State the blood parasite species.
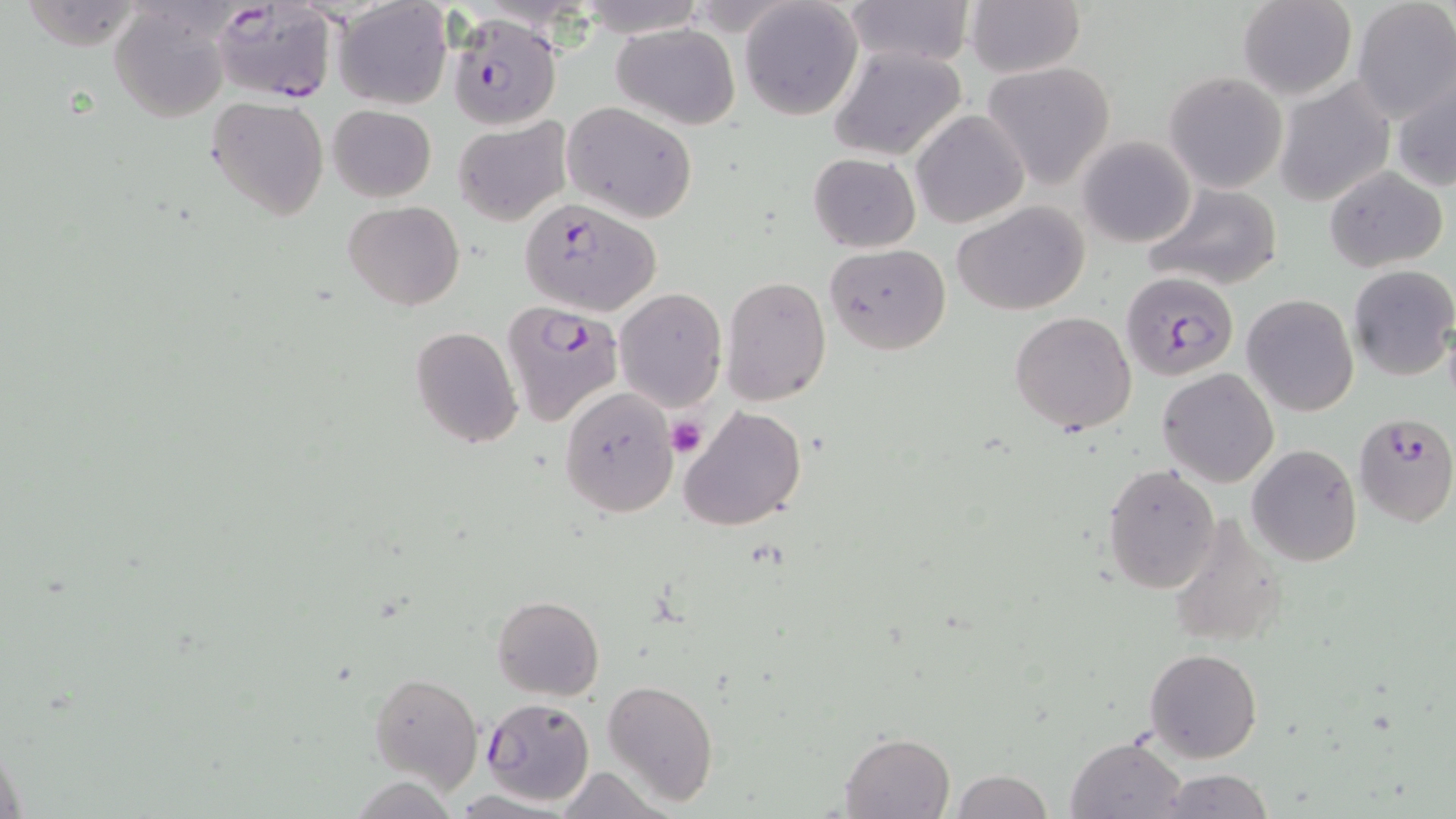

Plasmodium falciparum.

preparation = thin blood film
magnification = 1000x
Plasmodium falciparum-infected red blood cell locations = approximate bounding boxes as (x1, y1, x2, y2) in pixels: (212, 1, 339, 106), (447, 11, 560, 130), (520, 196, 661, 317), (1120, 271, 1240, 379), (502, 300, 625, 426), (1353, 410, 1456, 527), (479, 696, 595, 805)
field of view = single
modality = light microscopy
image size = 1456×819 pixels
platelet locations = approximate bounding boxes as (x1, y1, x2, y2) in pixels: (666, 416, 706, 456)
uninfected red blood cell locations = approximate bounding boxes as (x1, y1, x2, y2) in pixels: (19, 0, 148, 51), (841, 0, 975, 68), (1236, 0, 1357, 100), (333, 1, 453, 109), (740, 1, 863, 120), (964, 1, 1086, 79), (1351, 1, 1455, 124), (108, 5, 231, 123), (611, 24, 739, 129), (828, 45, 968, 161), (983, 63, 1115, 188), (1164, 71, 1287, 193), (1389, 72, 1456, 196), (1274, 77, 1397, 207), (207, 97, 328, 220), (562, 102, 697, 224), (327, 105, 436, 202), (911, 110, 1028, 228), (452, 117, 570, 226), (1078, 135, 1196, 247), (807, 152, 921, 252), (1323, 164, 1448, 272), (1141, 182, 1284, 292), (953, 200, 1091, 316), (344, 202, 464, 311), (824, 244, 951, 353), (1347, 264, 1456, 380), (721, 276, 832, 405), (613, 287, 726, 411), (1242, 293, 1359, 418), (1009, 312, 1136, 434), (411, 327, 523, 448), (1158, 368, 1279, 487), (559, 388, 681, 517), (678, 406, 806, 533), (1247, 444, 1362, 567), (1101, 463, 1220, 595), (1166, 513, 1287, 650), (491, 594, 604, 700), (1145, 647, 1262, 763), (369, 671, 484, 792), (603, 678, 719, 806), (840, 732, 953, 819), (1065, 735, 1189, 819), (550, 768, 663, 818), (1154, 768, 1274, 819), (951, 769, 1052, 819)
stain = May-Grünwald-Giemsa